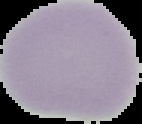
image size = 142×124 pixels
preparation = thin blood film
malaria status = uninfected
image type = cell region segmented out of the field of view; surrounding area masked to black